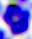
A leukocyte is seen. Micrograph. 400x magnification.